Give the extent of all uninfected red blood cells.
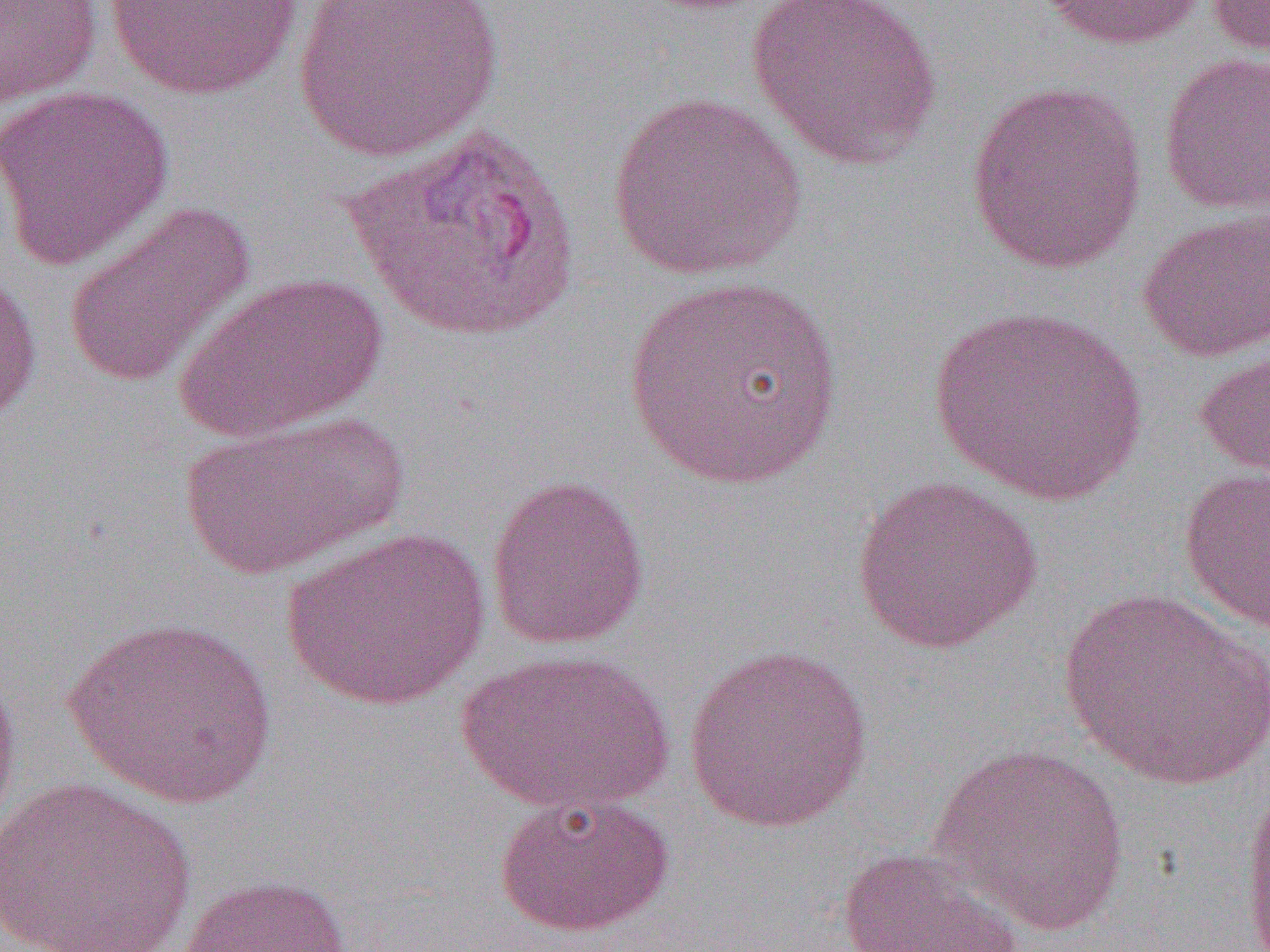
Approximate bounding boxes as (x1,y1)-(x2,y2) corner pairs in pixels.
Uninfected red blood cells: (0,0)-(103,109), (293,0)-(502,162), (747,0)-(946,171), (1037,0)-(1208,50), (1204,0)-(1270,60), (105,1)-(305,100), (1157,51)-(1270,215), (964,78)-(1149,274), (0,83)-(174,271), (607,90)-(808,282), (342,125)-(581,340), (61,200)-(257,390), (1137,207)-(1270,363), (0,256)-(42,427), (173,271)-(387,444), (625,273)-(842,490), (927,306)-(1149,507), (1194,329)-(1270,494), (178,408)-(408,578), (1178,467)-(1270,636), (485,473)-(651,650), (849,474)-(1044,653), (281,527)-(491,710), (1058,588)-(1270,790), (61,614)-(277,809), (682,642)-(875,834), (454,648)-(675,817), (0,655)-(21,847), (928,740)-(1129,936), (1238,772)-(1270,952), (2,776)-(199,952), (493,793)-(676,937), (836,847)-(1025,952), (175,873)-(352,952).

Slide-level diagnosis: Plasmodium vivax. Image is 1270×952 pixels. 1000x magnification. Thin blood smear. Optical microscopy. Single field of view.